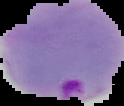

Summary:
  - Preparation: thin blood smear
  - Image type: segmented cell region with the area outside set to black
  - Image size: 124×106 pixels
  - Result: malaria parasites detected